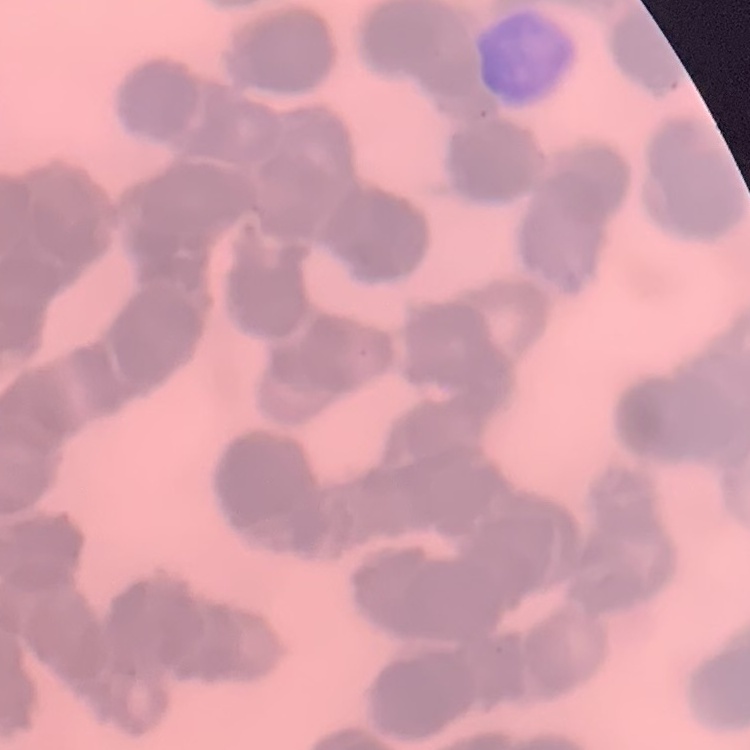
The erythrocytes exhibit rouleaux formation. Thin peripheral smear. Square crop of a larger photomicrograph. Stained with either Field's or Giemsa.